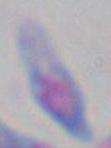

{
  "magnification": "1000x",
  "modality": "photomicrograph",
  "identification": "Toxoplasma gondii"
}